Report the malaria status of this cell.
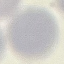

It is uninfected.

Summary:
  - Image type: cell patch, automatically extracted from a larger field of view and resized to 64 × 64 pixels
  - Capture: smartphone through the microscope eyepiece
  - Preparation: thin smear
  - Stain: Giemsa